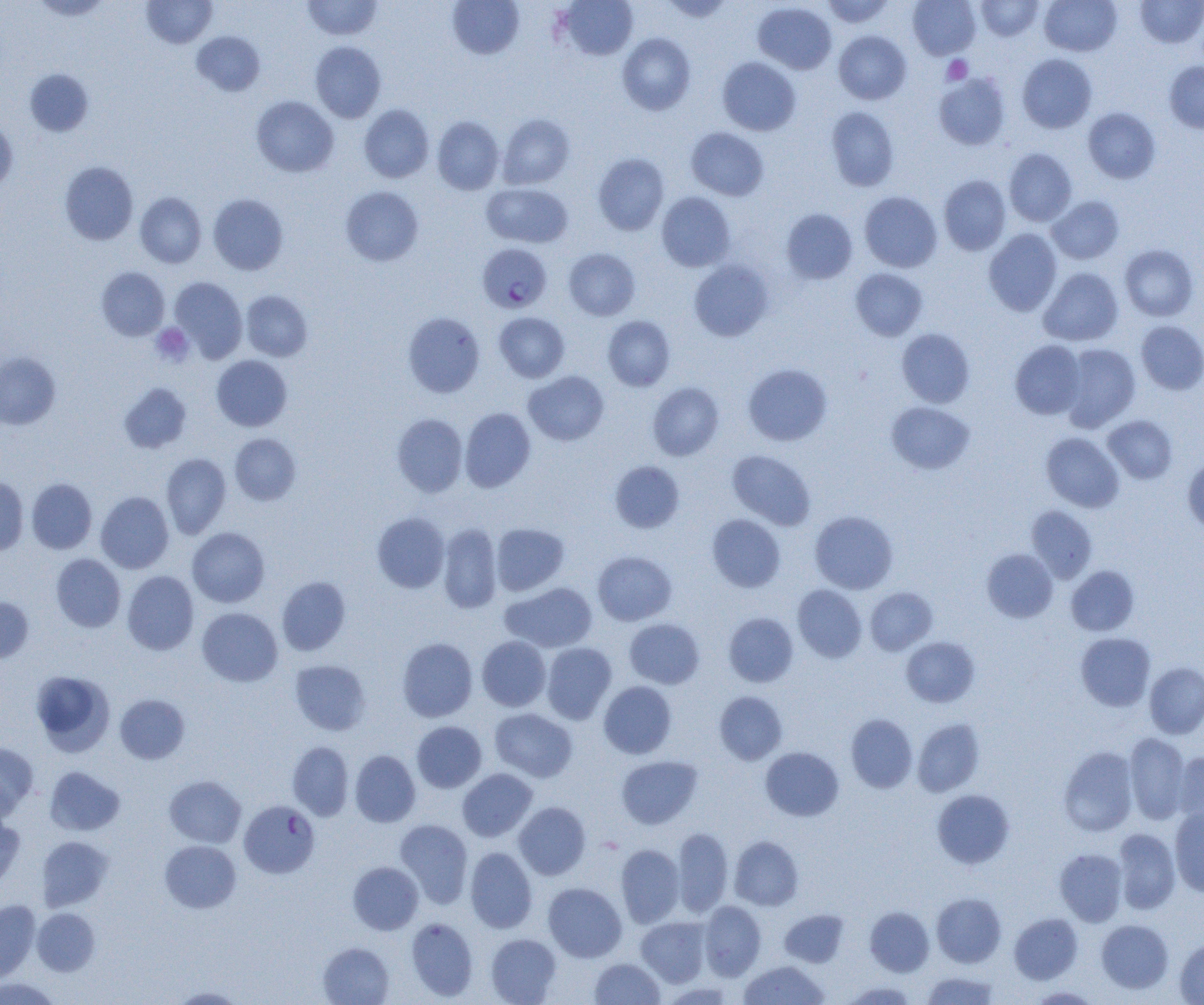

slide-level diagnosis = Plasmodium falciparum
image size = 1204×1005 pixels
uninfected red blood cell locations = approximate bounding boxes as (x1, y1, x2, y2) in pixels: (31, 0, 112, 20), (142, 0, 217, 48), (447, 0, 524, 60), (559, 0, 638, 60), (660, 0, 733, 23), (821, 0, 895, 28), (908, 0, 980, 60), (975, 0, 1044, 41), (1040, 0, 1121, 56), (1135, 0, 1204, 47), (302, 1, 383, 40), (753, 2, 836, 74), (192, 31, 265, 96), (834, 31, 912, 104), (617, 33, 696, 115), (310, 41, 386, 122), (1017, 54, 1097, 133), (717, 57, 801, 136), (1164, 61, 1204, 133), (24, 68, 94, 136), (934, 73, 1010, 150), (252, 96, 339, 177), (359, 104, 434, 183), (826, 106, 899, 191), (1083, 108, 1160, 184), (497, 113, 575, 189), (432, 116, 504, 194), (0, 121, 17, 194), (686, 127, 769, 201), (1003, 149, 1077, 226), (593, 153, 669, 235), (59, 162, 138, 245), (939, 175, 1011, 255), (481, 182, 573, 248), (340, 186, 424, 266), (859, 191, 942, 272), (135, 192, 206, 268), (657, 192, 736, 271), (208, 194, 289, 275), (1047, 196, 1124, 264), (781, 208, 857, 284), (983, 229, 1062, 316), (1119, 244, 1199, 321), (564, 248, 640, 321), (688, 259, 773, 341), (96, 267, 169, 340), (1038, 267, 1123, 346), (850, 268, 927, 341), (169, 276, 247, 362), (240, 290, 312, 361), (494, 312, 569, 382), (403, 313, 485, 397), (603, 315, 675, 391), (1136, 320, 1204, 395), (897, 328, 975, 407), (1010, 340, 1086, 419), (1060, 344, 1140, 432), (0, 352, 61, 430), (211, 355, 292, 431), (742, 363, 832, 446), (524, 371, 608, 446), (119, 382, 191, 453), (648, 382, 724, 461), (886, 401, 975, 474), (459, 407, 536, 492), (392, 413, 468, 497), (1103, 415, 1177, 484), (1041, 432, 1124, 512), (229, 433, 301, 505), (727, 449, 816, 530), (161, 453, 231, 539), (1182, 455, 1204, 533), (610, 460, 684, 533), (0, 476, 28, 556), (27, 478, 97, 554), (96, 491, 174, 573), (1026, 505, 1097, 582), (810, 511, 898, 594), (372, 512, 450, 594), (707, 514, 786, 592), (438, 523, 502, 613), (491, 523, 569, 595), (187, 527, 270, 608), (982, 548, 1058, 623), (593, 551, 677, 625), (51, 553, 125, 632), (1066, 565, 1139, 636), (122, 571, 199, 655), (277, 576, 351, 656), (501, 582, 597, 652), (793, 584, 867, 663), (865, 587, 937, 655), (0, 597, 33, 664), (197, 607, 283, 686), (724, 612, 798, 687), (624, 618, 704, 689), (1076, 633, 1155, 711), (477, 636, 551, 711), (901, 636, 979, 707), (397, 637, 478, 722), (542, 642, 617, 724), (290, 660, 371, 735), (1145, 662, 1204, 739), (31, 669, 115, 756), (599, 681, 677, 759), (714, 691, 787, 764), (115, 694, 190, 764), (489, 708, 577, 782), (845, 713, 917, 793), (912, 718, 984, 797), (411, 721, 487, 792), (1124, 733, 1190, 823), (0, 741, 39, 819), (287, 741, 354, 820), (1058, 746, 1138, 836), (761, 747, 844, 821), (350, 750, 421, 827), (1173, 750, 1204, 825), (617, 756, 702, 829), (44, 766, 125, 836), (457, 768, 537, 842), (164, 775, 246, 848), (932, 789, 1014, 869), (514, 802, 590, 879), (1169, 808, 1204, 896), (0, 812, 25, 890), (394, 818, 473, 908), (672, 828, 733, 916), (1113, 828, 1180, 914), (729, 835, 804, 911), (37, 836, 114, 911), (160, 840, 241, 913), (616, 844, 684, 927), (465, 847, 537, 933), (1055, 848, 1127, 926), (348, 861, 423, 934), (543, 882, 627, 962), (932, 892, 1006, 967), (0, 900, 40, 981), (699, 901, 766, 980), (865, 906, 934, 976), (32, 908, 100, 976), (779, 909, 849, 967), (1009, 913, 1082, 984), (636, 916, 711, 987), (406, 917, 478, 1001), (1096, 919, 1173, 993), (485, 933, 561, 1004), (1175, 938, 1204, 1005), (318, 942, 394, 1005), (590, 958, 665, 1004), (739, 961, 828, 1004), (920, 972, 1000, 1004), (0, 977, 61, 1005), (840, 980, 919, 1004), (167, 986, 248, 1004), (1026, 986, 1100, 1004)
platelet locations = approximate bounding boxes as (x1, y1, x2, y2) in pixels: (942, 55, 973, 84), (151, 323, 194, 366)
magnification = 1000x
modality = light microscopy
preparation = thin blood smear
field of view = single
Plasmodium falciparum-infected red blood cell locations = approximate bounding boxes as (x1, y1, x2, y2) in pixels: (477, 243, 552, 313), (239, 799, 320, 878)